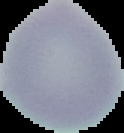
Summary:
  - Image size: 124×133 pixels
  - Preparation: thin blood smear
  - Image type: segmented cell region on a black background
  - Malaria status: uninfected